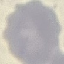

result: negative for malaria parasites
stain: Giemsa
capture: smartphone through the microscope eyepiece
preparation: thin smear
image_type: cell patch, automatically extracted from a larger field of view and resized to 64 × 64 pixels